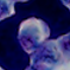

Summary:
  - Magnification: 1000x
  - Identification: leukocyte
  - Modality: photomicrograph